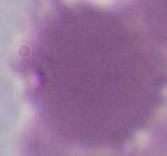
magnification = 1000x
modality = photomicrograph
identification = red blood cell